Find each parasitized red blood cell.
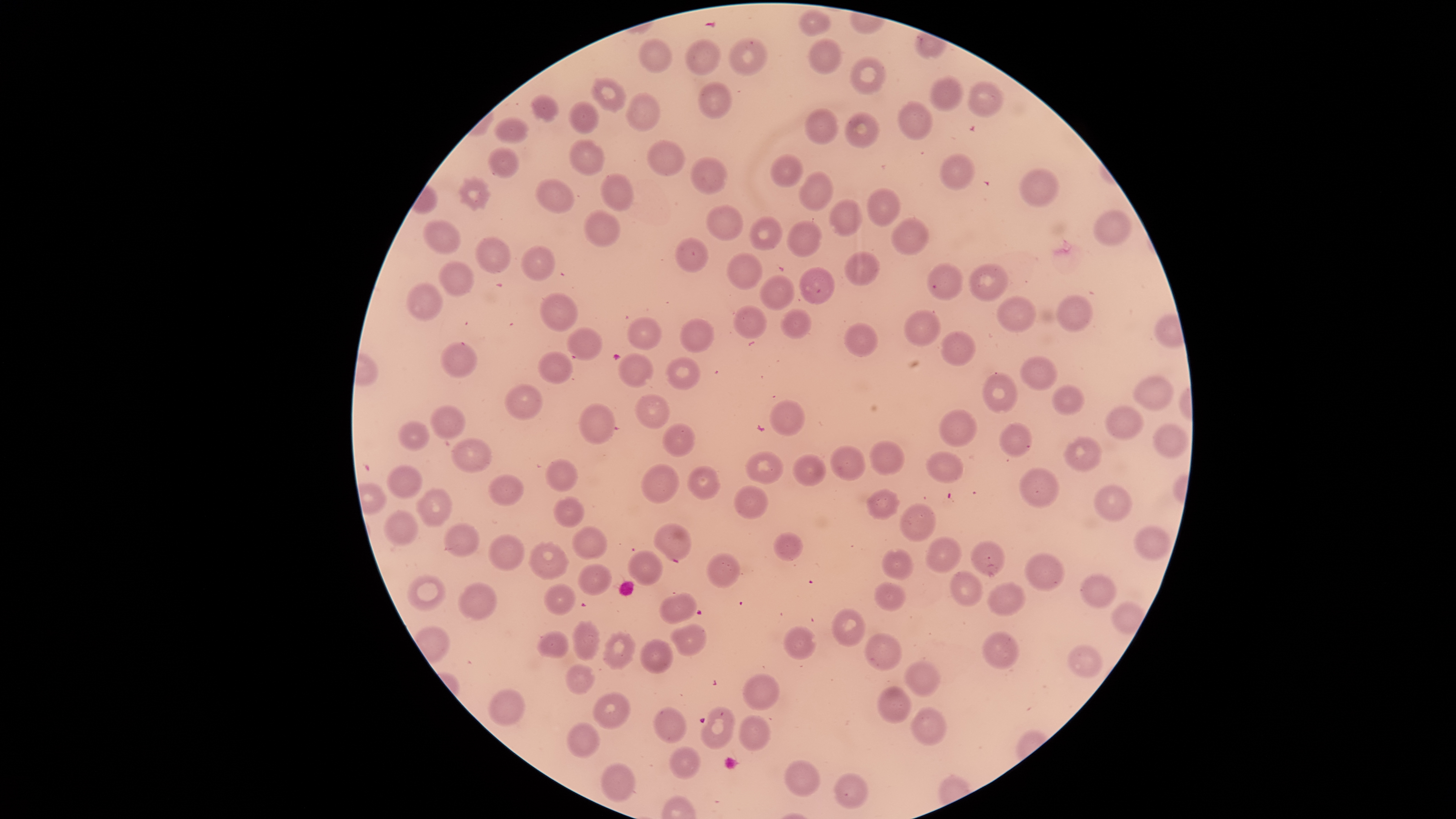

No parasitized red blood cells identified.

{
  "preparation": "thin blood smear",
  "field_of_view": "single",
  "uninfected_red_blood_cells": "approximate bounding boxes as {left, top, right, bottom} in pixels: {796, 9, 831, 36}, {729, 37, 768, 76}, {639, 38, 673, 73}, {685, 38, 721, 75}, {809, 39, 842, 75}, {851, 55, 886, 94}, {930, 75, 964, 111}, {593, 78, 627, 112}, {698, 81, 733, 119}, {969, 82, 1004, 117}, {626, 93, 660, 132}, {532, 95, 559, 121}, {899, 101, 932, 141}, {569, 102, 600, 133}, {806, 108, 838, 145}, {846, 111, 880, 148}, {494, 116, 529, 143}, {569, 138, 606, 175}, {648, 140, 686, 175}, {487, 146, 521, 179}, {940, 153, 974, 191}, {770, 154, 804, 187}, {689, 156, 726, 193}, {1019, 166, 1060, 208}, {800, 171, 834, 212}, {601, 173, 633, 211}, {459, 178, 488, 207}, {536, 178, 574, 213}, {866, 188, 901, 227}, {829, 199, 863, 236}, {705, 204, 744, 241}, {1092, 209, 1132, 247}, {585, 210, 619, 246}, {749, 216, 783, 250}, {892, 216, 928, 254}, {423, 219, 460, 253}, {787, 220, 821, 256}, {476, 237, 511, 271}, {673, 238, 709, 271}, {521, 246, 554, 280}, {845, 251, 881, 286}, {727, 252, 762, 289}, {439, 261, 475, 297}, {926, 263, 963, 300}, {969, 263, 1009, 302}, {800, 267, 834, 304}, {758, 274, 797, 311}, {406, 283, 443, 322}, {539, 293, 578, 331}, {997, 295, 1036, 332}, {1057, 296, 1093, 331}, {733, 305, 766, 338}, {781, 309, 811, 339}, {904, 309, 940, 346}, {627, 317, 662, 349}, {680, 318, 715, 352}, {844, 322, 878, 357}, {567, 327, 604, 360}, {940, 330, 975, 365}, {440, 342, 478, 380}, {538, 350, 572, 384}, {617, 352, 654, 388}, {1021, 355, 1058, 390}, {666, 357, 701, 390}, {984, 373, 1018, 412}, {1133, 374, 1174, 412}, {505, 383, 543, 420}, {1052, 386, 1085, 415}, {636, 394, 669, 429}, {769, 399, 804, 436}, {580, 403, 615, 445}, {430, 405, 467, 440}, {1106, 405, 1143, 439}, {938, 409, 977, 449}, {399, 421, 429, 451}, {998, 422, 1032, 457}, {663, 423, 695, 458}, {1153, 423, 1188, 457}, {1064, 437, 1102, 471}, {450, 438, 492, 472}, {869, 439, 905, 476}, {830, 445, 865, 482}, {747, 450, 782, 484}, {925, 451, 964, 485}, {793, 454, 826, 486}, {547, 458, 578, 491}, {640, 463, 678, 503}, {387, 465, 423, 499}, {689, 466, 719, 499}, {1019, 467, 1060, 507}, {490, 474, 523, 505}, {1094, 485, 1132, 521}, {735, 486, 768, 519}, {417, 488, 452, 527}, {866, 488, 901, 520}, {554, 498, 585, 527}, {900, 503, 936, 542}, {383, 510, 418, 545}, {444, 523, 479, 557}, {655, 523, 692, 561}, {1134, 524, 1171, 560}, {573, 525, 607, 559}, {774, 532, 803, 562}, {489, 534, 525, 571}, {926, 537, 963, 573}, {971, 541, 1004, 575}, {529, 542, 568, 578}, {627, 549, 662, 585}, {883, 549, 913, 580}, {708, 552, 740, 588}, {1026, 552, 1064, 591}, {578, 562, 611, 595}, {950, 570, 981, 607}, {1080, 573, 1116, 608}, {407, 574, 446, 611}, {458, 582, 497, 620}, {874, 582, 905, 611}, {986, 582, 1025, 616}, {546, 583, 576, 615}, {661, 592, 697, 624}, {832, 609, 865, 646}, {573, 622, 599, 661}, {669, 623, 706, 656}, {783, 625, 815, 660}, {538, 631, 568, 660}, {983, 631, 1021, 668}, {603, 632, 634, 669}, {865, 634, 903, 671}, {641, 639, 673, 672}, {1068, 645, 1102, 678}, {905, 660, 942, 695}, {565, 664, 594, 694}, {742, 674, 779, 711}, {878, 686, 912, 724}, {488, 689, 525, 726}, {593, 692, 630, 730}, {911, 706, 947, 745}, {654, 707, 686, 743}, {701, 707, 734, 750}, {740, 715, 770, 751}, {567, 722, 600, 758}, {669, 746, 700, 780}, {785, 758, 821, 795}, {600, 762, 636, 802}, {832, 773, 867, 809}",
  "image_size": "1456×819 pixels",
  "stain": "Giemsa",
  "visible_region": "circular",
  "capture": "smartphone photograph through the microscope eyepiece"
}